Describe the morphology of the red blood cells.
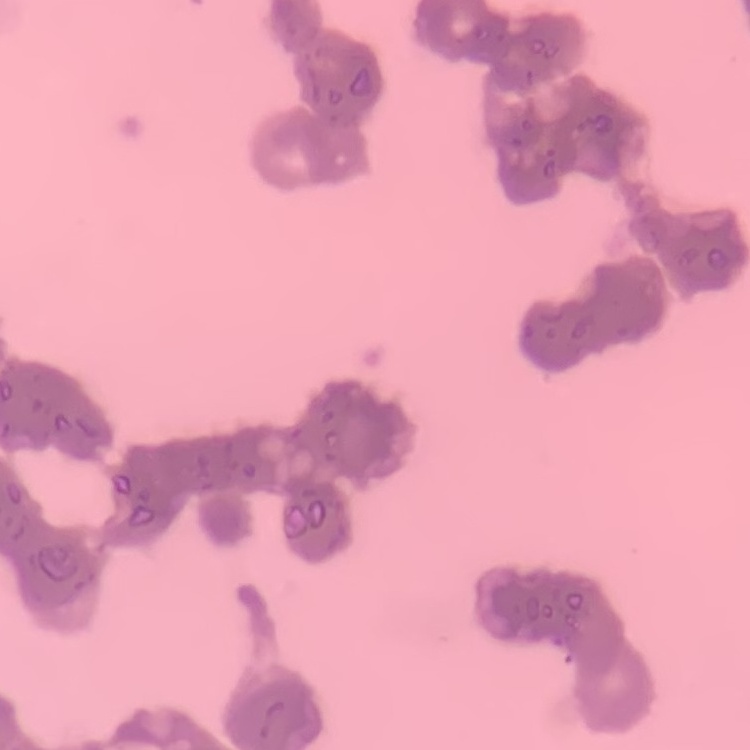
They show rouleaux formation.

{
  "stain": "Field's or Giemsa",
  "image_type": "one tile cut from a larger photomicrograph",
  "preparation": "thin blood smear"
}